Assess the morphology of the erythrocytes.
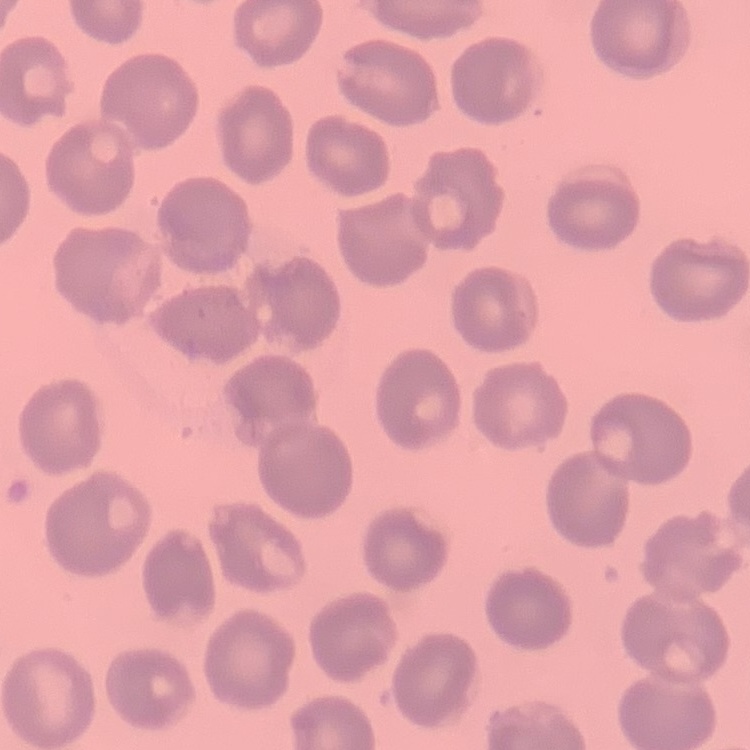

No rouleaux formation.

Summary:
  - Image type: square crop of a larger photomicrograph
  - Preparation: thin blood film
  - Stain: Field's or Giemsa